Assess this cell for malaria.
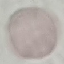

It is uninfected.

Summary:
  - Preparation: thin smear
  - Stain: Giemsa
  - Image type: cell patch, automatically extracted from a larger field of view and resized to 64 × 64 pixels
  - Capture: smartphone camera at the microscope eyepiece